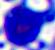
identification: leukocyte
magnification: 400x
modality: micrograph